Name the parasite shown.
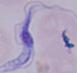
This is a trypanosome.

Summary:
  - Modality: photomicrograph
  - Magnification: 1000x